Report the malaria status.
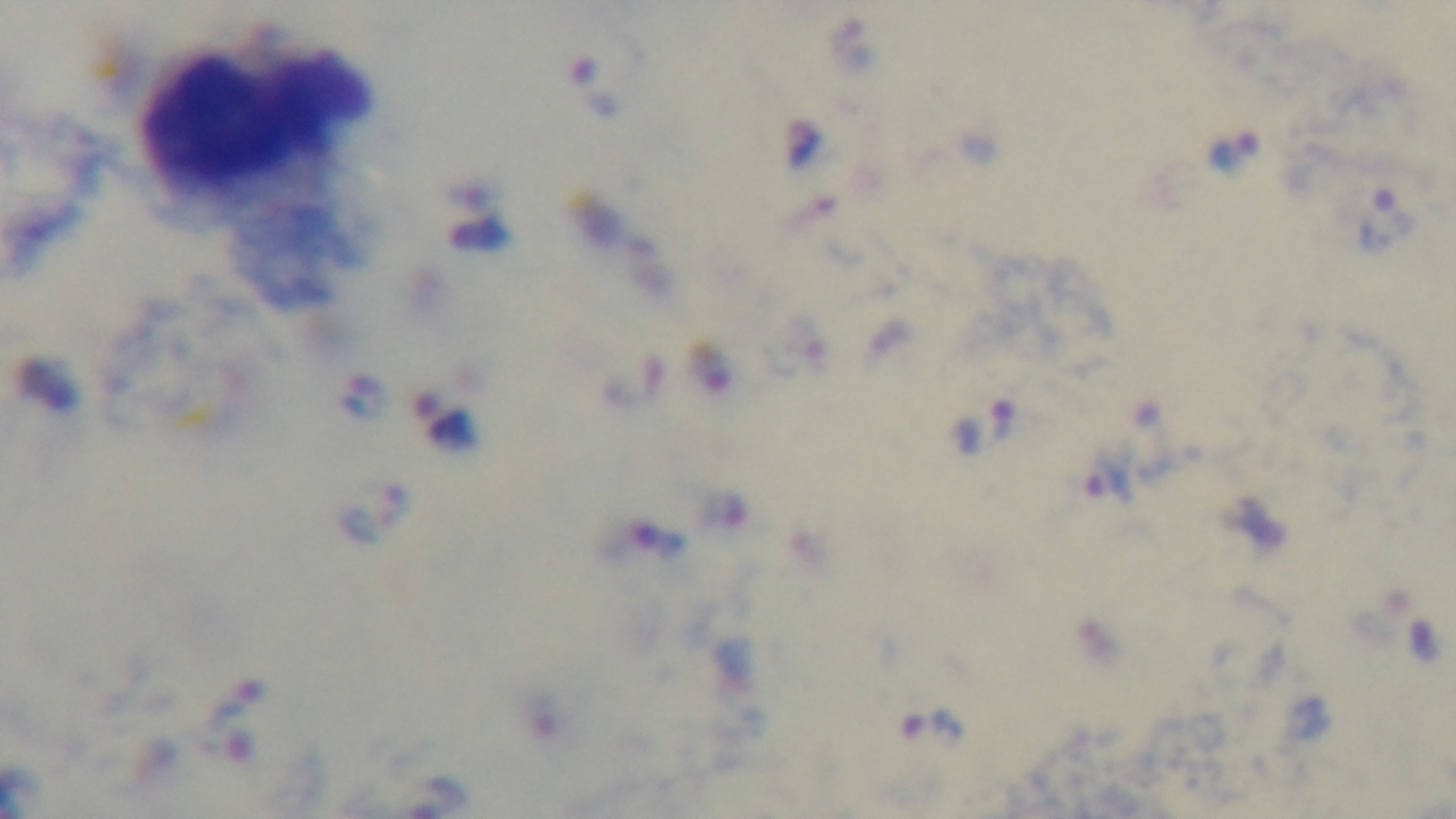

It is infected.

preparation = thick smear
stain = Giemsa
objective = 100x oil immersion
field of view = one from the slide
capture = mounted 4K digital camera
modality = light microscopy